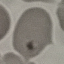

malaria status = parasitized
capture = smartphone camera at the microscope eyepiece
image type = cell patch, automatically extracted from a larger field of view and resized to 64 × 64 pixels
preparation = thin smear
stain = Giemsa